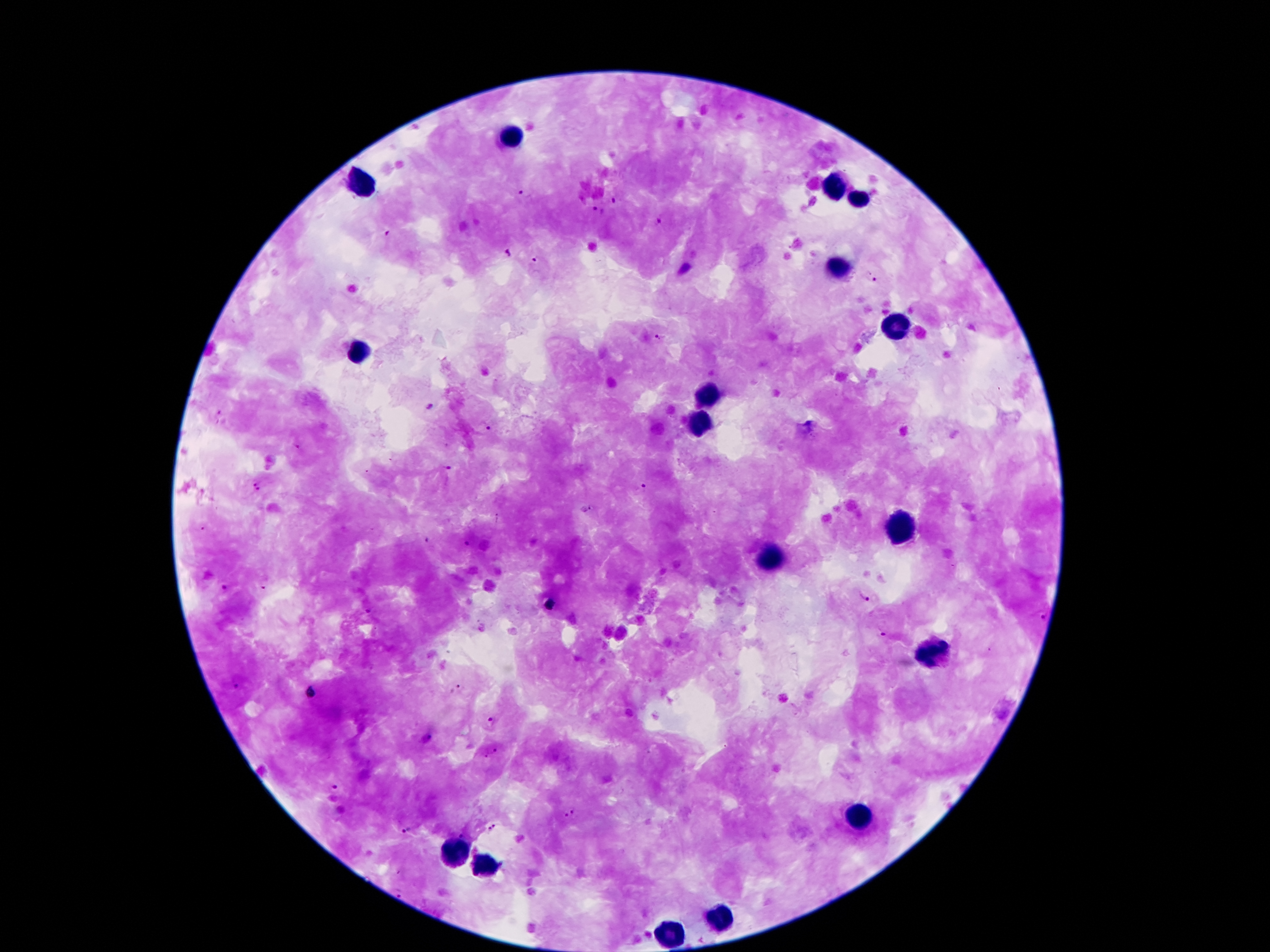 Approximate centers as (x, y) in pixels. Malaria parasite locations: (526, 196), (613, 200), (598, 212), (658, 222), (388, 235), (508, 253), (530, 260), (871, 278), (659, 338), (430, 407), (485, 429), (448, 467), (255, 481), (259, 491), (642, 491), (586, 510), (204, 530), (427, 541), (467, 545), (263, 588), (226, 589), (862, 595), (549, 606), (1044, 616), (882, 635), (235, 687), (459, 688), (310, 692), (491, 721), (429, 737), (495, 751), (486, 756), (336, 787), (574, 809), (563, 815), (493, 826), (405, 830), (463, 832), (398, 893). Leukocyte locations: (513, 137), (361, 185), (833, 187), (857, 201), (833, 267), (895, 328), (361, 349), (711, 393), (701, 423), (897, 528), (769, 556), (935, 656), (861, 819), (451, 853), (485, 866), (717, 919), (671, 935). Single field of view. Smartphone photograph taken through the microscope eyepiece. Giemsa stain. Image is 1270×952 pixels. Patient malaria status: infected with Plasmodium falciparum. 100x magnification. Thick blood film.